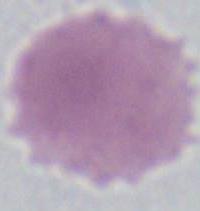

Summary:
  - Modality: micrograph
  - Magnification: 1000x
  - Identification: red blood cell